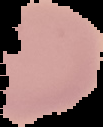
result = negative for malaria parasites
preparation = thin blood film
image size = 103×127 pixels
image type = cell region segmented out of the field of view; surrounding area masked to black